Identify the preparation type.
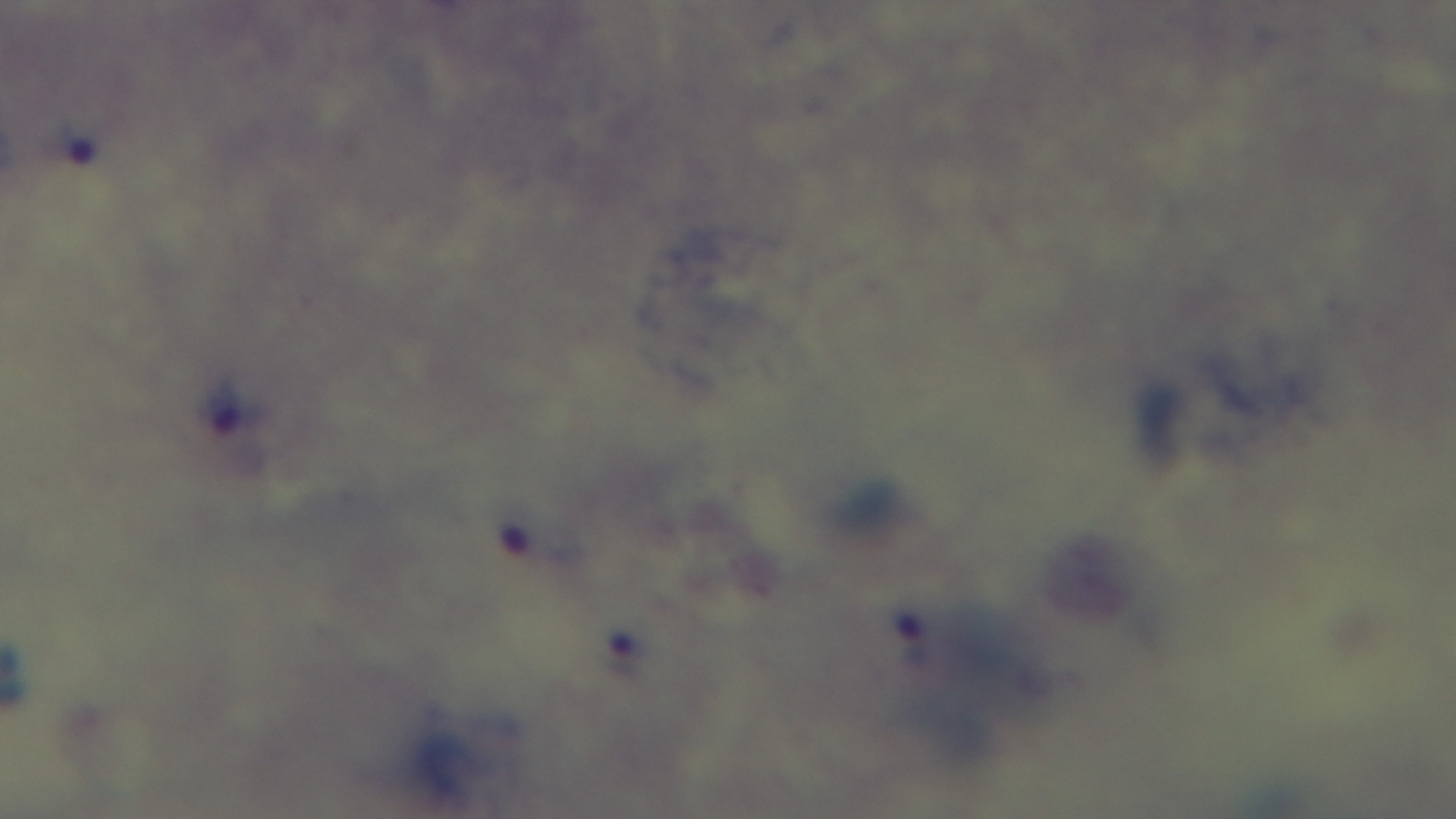
It is a thick blood film.

Oil-immersion objective, 100x. One field from the slide. Giemsa-stained. Malaria status: positive. Captured with a mounted 4K digital camera. Photomicrograph.